Name the cell type shown.
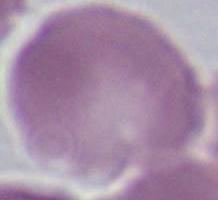

An erythrocyte.

Summary:
  - Modality: photomicrograph
  - Magnification: 1000x